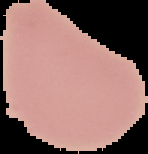
Summary:
  - Preparation: thin blood film
  - Result: no malaria parasites detected
  - Image type: segmented cell region with the area outside set to black
  - Image size: 148×154 pixels